Report the malaria status of this cell.
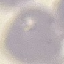

Uninfected.

Giemsa-stained preparation. Photographed with a smartphone camera at the microscope eyepiece. Cell patch, automatically extracted from a larger field of view and resized to 64 × 64 pixels. Thin blood smear.